Identify the cell.
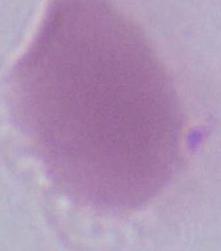

This is an erythrocyte.

Micrograph. 1000x magnification.